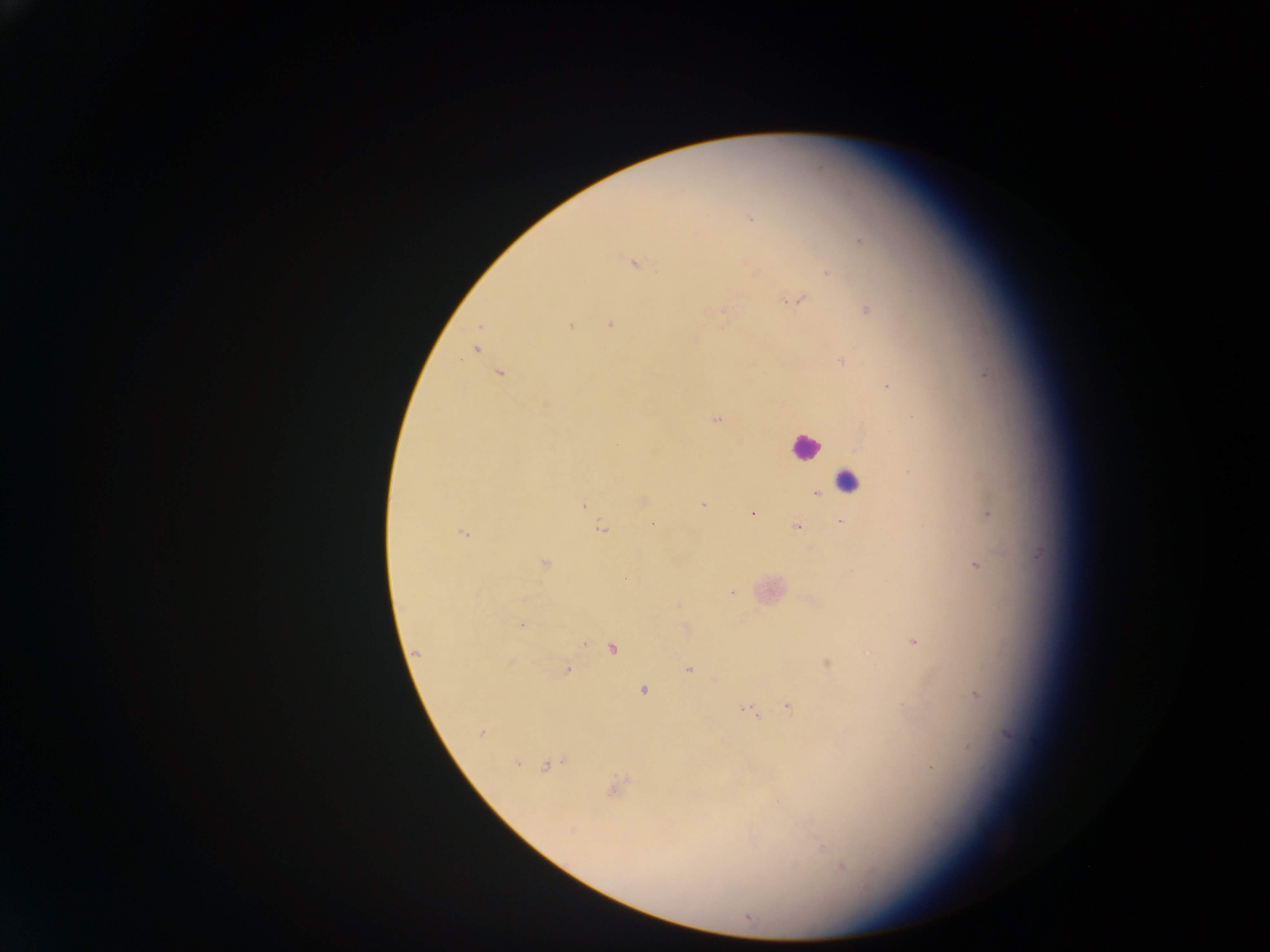
country = Ghana
preparation = thick blood smear
field of view = single
capture = mobile-phone photograph through a microscope
image size = 1270×952 pixels
leukocyte locations = approximate centers as [x, y] in pixels: [805, 445], [845, 483]
Plasmodium parasite locations = approximate centers as [x, y] in pixels: [751, 219], [861, 241], [633, 263], [826, 273], [795, 300], [868, 310], [724, 315], [610, 324], [571, 325], [694, 340], [476, 350], [843, 362], [500, 374], [887, 387], [716, 420], [817, 494], [643, 501], [583, 504], [703, 505], [988, 513], [752, 514], [840, 521], [653, 525], [797, 527], [601, 529], [463, 532], [544, 563], [976, 566], [731, 593], [679, 605], [521, 624], [913, 642], [584, 643], [613, 648], [417, 653], [828, 664], [566, 669], [689, 669], [643, 691], [976, 695], [788, 706], [750, 711], [481, 733], [516, 763], [548, 766], [615, 788], [573, 829], [822, 847], [842, 867], [748, 918]